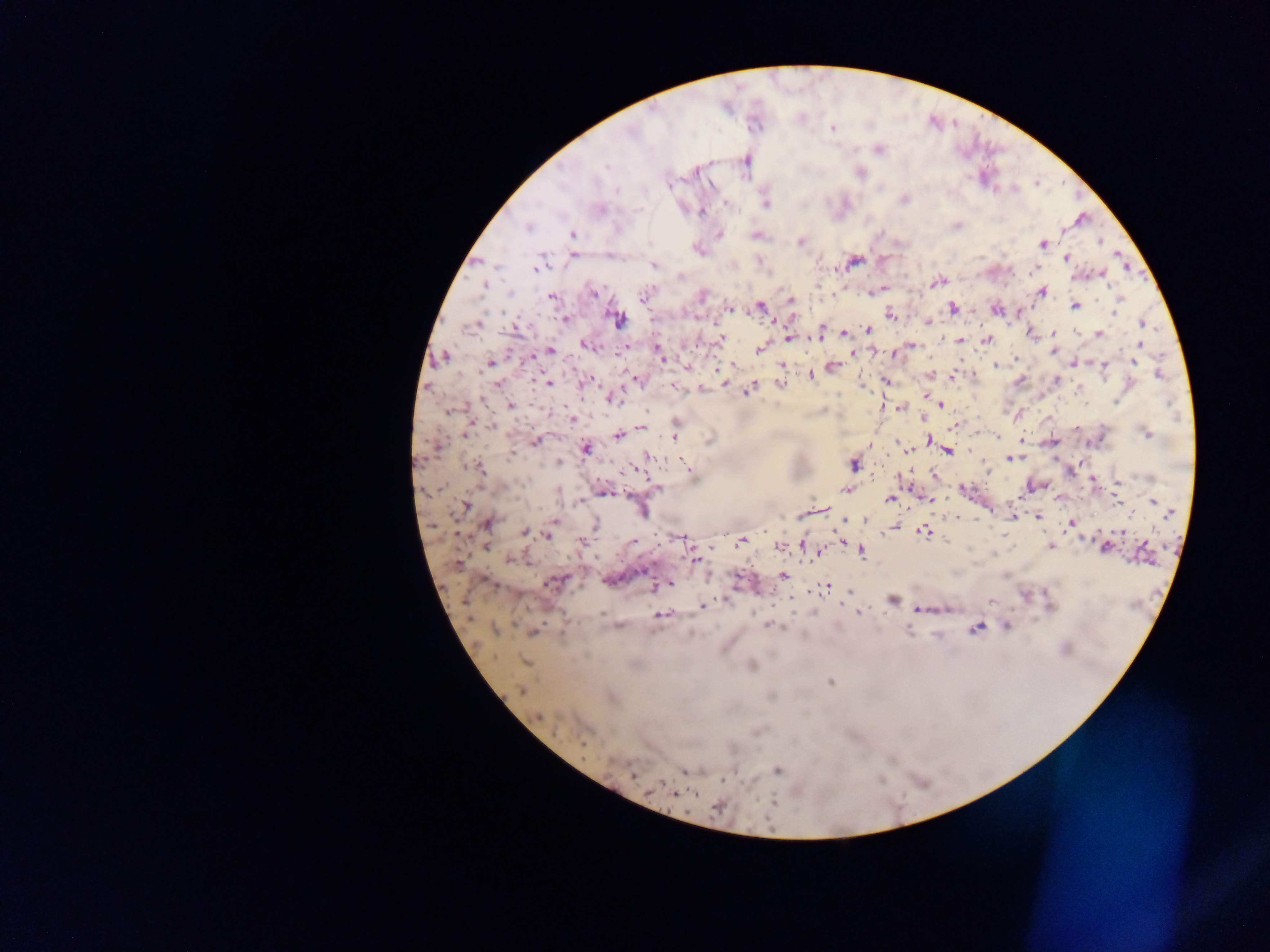

Approximate centers as x y in pixels.
Summary:
  - Malaria parasite locations: 832 128; 878 149; 606 166; 696 169; 860 174; 617 190; 905 200; 727 204; 765 204; 600 209; 702 212; 957 225; 527 226; 720 234; 572 235; 756 236; 1099 241; 800 242; 1043 244; 573 255; 1066 258; 853 262; 760 263; 654 265; 536 268; 1031 270; 1102 274; 680 276; 936 281; 484 287; 594 293; 1042 293; 643 295; 702 296; 551 297; 791 299; 1119 299; 1075 306; 761 307; 953 308; 730 309; 996 310; 1115 312; 890 315; 618 319; 564 320; 927 321; 1143 324; 473 326; 516 327; 868 329; 1075 332; 820 333; 845 333; 1030 333; 1053 333; 1099 334; 721 338; 790 338; 960 340; 987 340; 1141 345; 585 346; 911 346; 759 349; 550 350; 658 351; 894 352; 1052 352; 854 353; 661 356; 444 357; 1015 359; 1073 362; 1134 362; 490 363; 781 365; 996 365; 1104 365; 832 366; 720 368; 1160 375; 810 377; 951 377; 1056 379; 637 380; 886 381; 1019 381; 548 382; 726 383; 498 384; 781 384; 674 387; 701 388; 748 389; 1079 389; 926 395; 613 398; 1115 401; 940 404; 510 405; 900 408; 449 412; 924 417; 572 420; 491 426; 953 426; 640 428; 1077 428; 468 432; 1147 433; 465 434; 619 435; 674 436; 997 438; 929 440; 1022 440; 535 442; 899 444; 439 446; 585 448; 906 449; 947 450; 511 455; 648 457; 1012 459; 559 462; 853 464; 689 468; 478 469; 934 475; 1093 481; 1118 482; 656 488; 845 490; 964 490; 605 493; 889 499; 930 500; 1153 501; 1117 503; 465 506; 640 511; 1018 513; 1169 513; 1131 514; 1037 516; 865 519; 845 520; 978 520; 487 524; 553 524; 1070 524; 595 526; 893 527; 924 532; 1121 532; 525 533; 548 534; 679 538; 741 540; 581 541; 633 541; 1050 546; 485 547; 779 547; 804 547; 1105 548; 861 551; 695 558; 511 560; 783 577; 556 582; 666 585; 657 586; 826 588; 891 600; 992 601; 702 606; 920 610; 859 612; 660 616; 772 626; 1007 626; 976 628; 494 629; 533 633; 525 662; 751 665; 831 682; 522 691; 772 696; 539 716; 584 743; 689 769; 776 771; 633 775; 674 793; 718 807
  - Capture: mobile-phone photograph through a microscope
  - Image size: 1270×952 pixels
  - Field of view: single
  - Country: Ghana
  - Preparation: thick blood film